Classify this cell by malaria status.
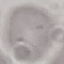
Uninfected.

Thin blood smear. Acquired by smartphone through the microscope eyepiece. Automatically extracted cell patch, resized to 64 × 64 pixels. Giemsa-stained preparation.